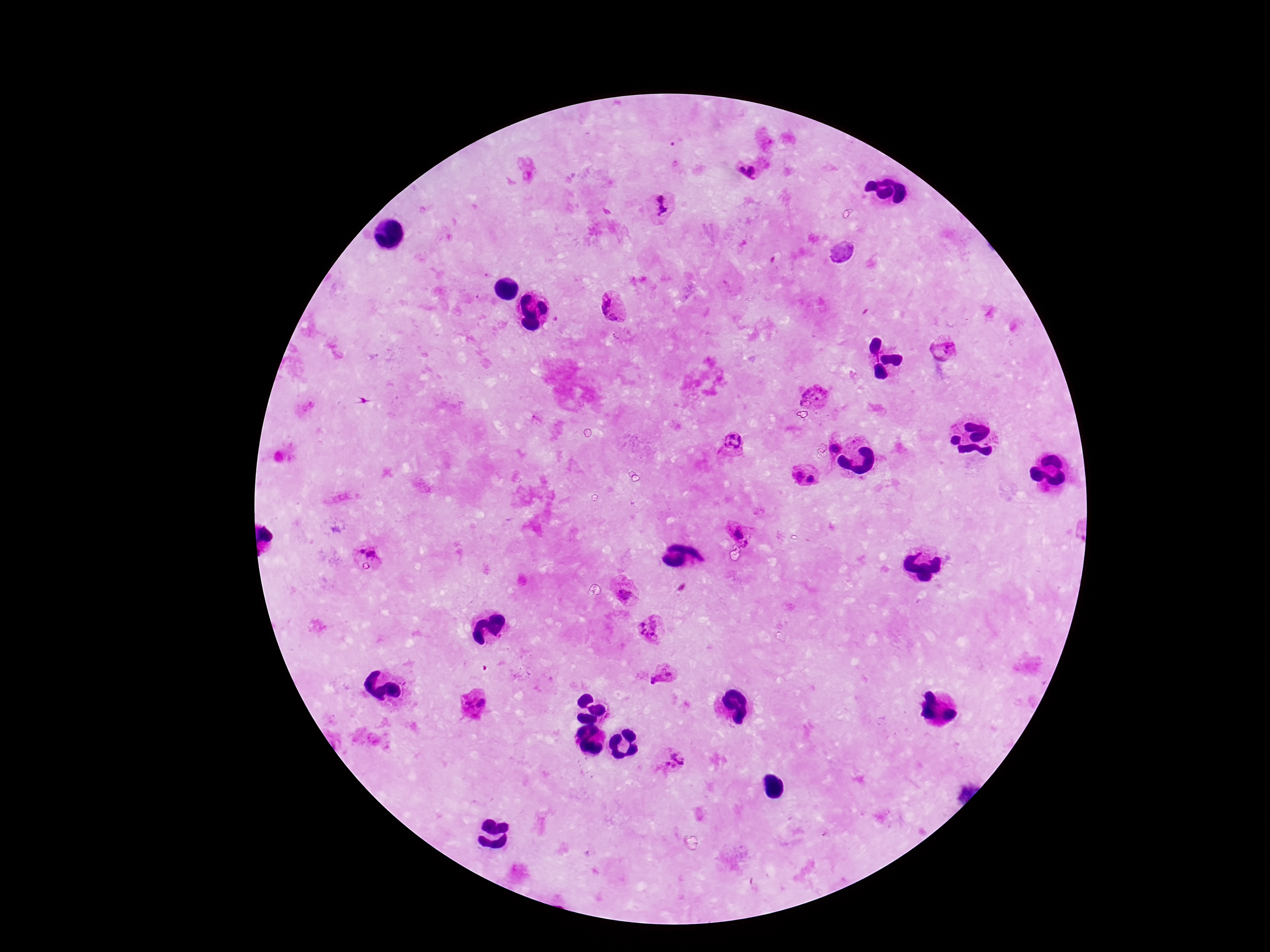

Approximate centers as [x, y] in pixels. Plasmodium parasite locations: [741, 171], [753, 172], [664, 204], [613, 308], [944, 348], [815, 395], [732, 440], [837, 447], [798, 474], [811, 478], [738, 534], [361, 552], [373, 554], [626, 592], [650, 626], [662, 675], [475, 700], [672, 762]. Patient malaria status: positive. 100x magnification. Single field of view. Smartphone photograph taken through the microscope eyepiece. Thick blood film. Giemsa-stained preparation. Image is 1270×952 pixels.